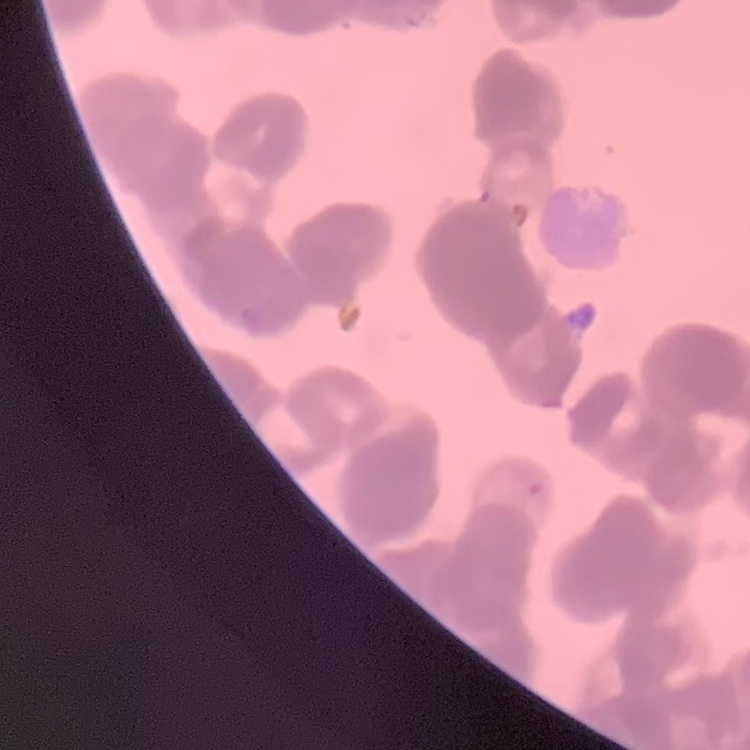

erythrocyte morphology = rouleaux formation
preparation = thin blood smear
stain = Field's or Giemsa
image type = square crop of a larger photomicrograph